Point out each malaria parasite and classify it by life-cycle stage.
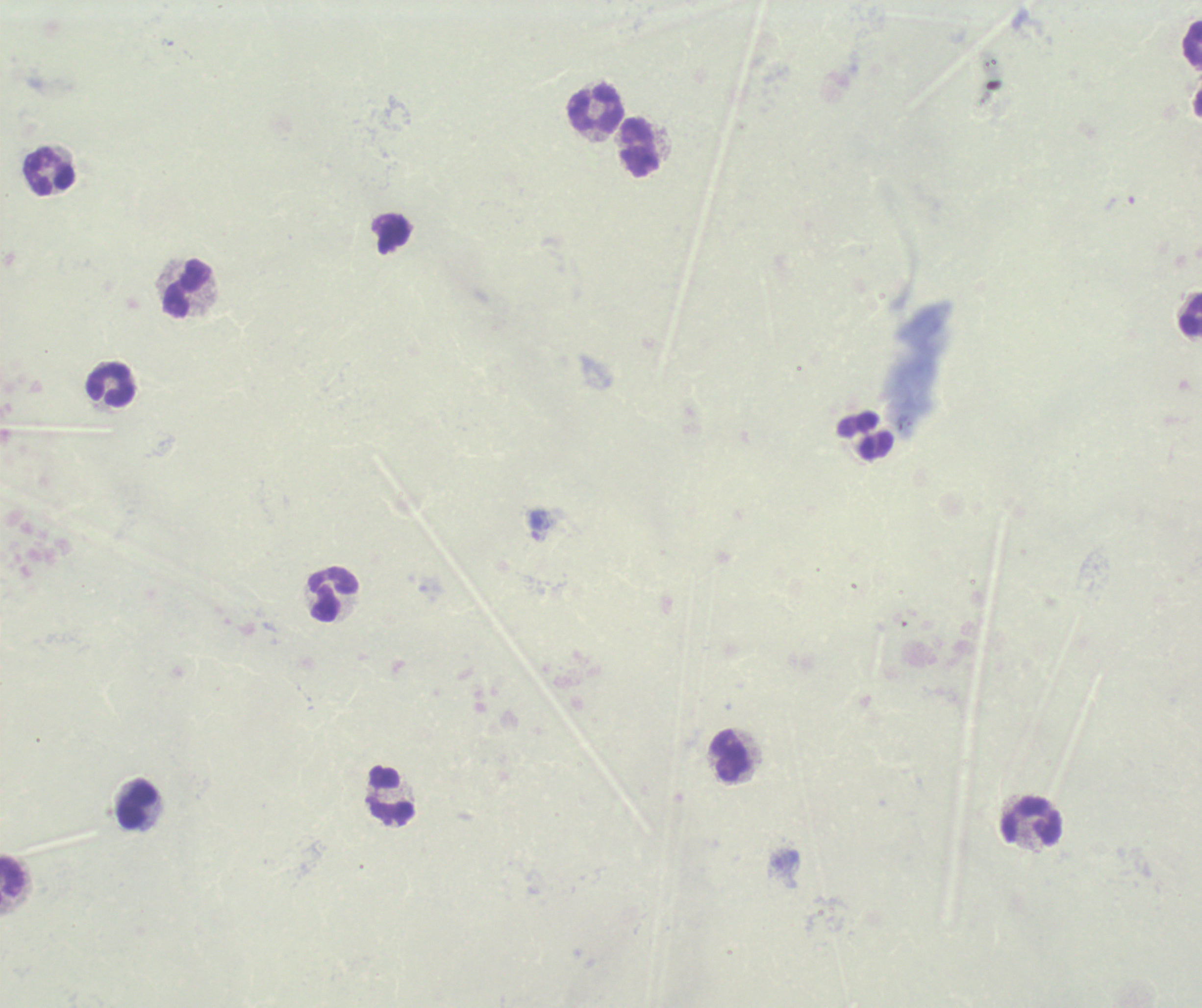

Negative for malaria parasites.

coordinate format = approximate centers as (x, y) in pixels
leukocyte locations = (1193, 44), (598, 107), (640, 148), (51, 172), (188, 290), (1191, 315), (112, 385), (865, 436), (334, 596), (731, 755), (391, 796), (138, 806), (1032, 821), (12, 878)
preparation = thick smear of blood
magnification = 100x
background quality = unsatisfactory
context = previously used in an actual diagnosis
stain = Romanowsky
image size = 1202×1008 pixels
field of view = one from this slide